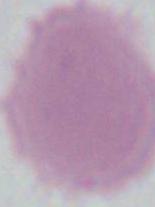

Captured at 1000x magnification. An erythrocyte is seen. Micrograph.